Report the malaria status of this cell.
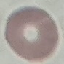

It is uninfected.

Photographed with a smartphone camera at the microscope eyepiece. Thin smear of blood. Automatically extracted cell patch, resized to 64 × 64 pixels. Giemsa-stained preparation.